Classify this cell by malaria status.
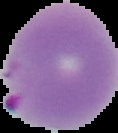
Parasitized.

Summary:
  - Image type: segmented cell region on a black background
  - Preparation: thin blood smear
  - Image size: 118×133 pixels